Assess this cell for malaria.
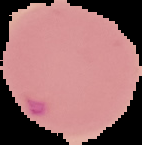
Parasitized.

Summary:
  - Image type: segmented cell region with the area outside set to black
  - Preparation: thin blood smear
  - Image size: 142×145 pixels